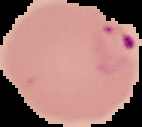 Segmented cell region on a black background. Image is 142×127 pixels. Malaria status: parasitized. From a thin blood smear.